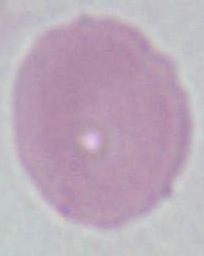 Photomicrograph. A red blood cell is shown. Captured at 1000x magnification.